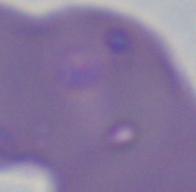
magnification: 1000x
identification: Babesia
modality: micrograph